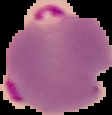
From a thin blood smear. Image is 112×115 pixels. Result: Plasmodium parasites detected. Segmented cell region on a black background.